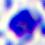

Summary:
  - Magnification: 400x
  - Identification: white blood cell
  - Modality: photomicrograph